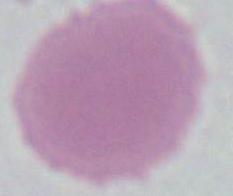
An erythrocyte is shown. Captured at 1000x magnification. Photomicrograph.